Outline each blood parasite and name the species.
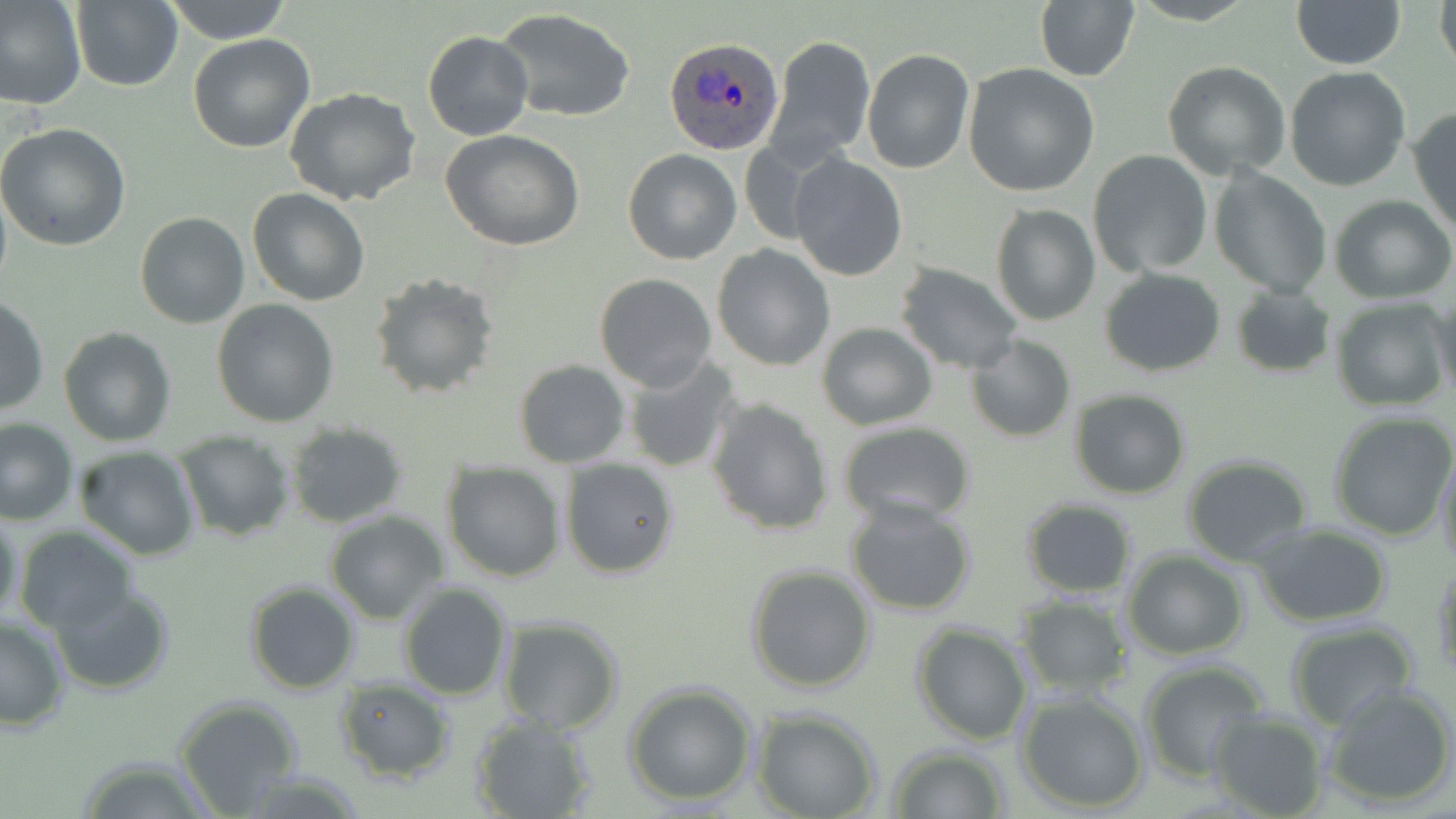

Approximate bounding boxes as named x1/y1/x2/y2 corners in pixels.
Plasmodium ovale-infected red blood cells: (x1=664, y1=37, x2=785, y2=156).
No Plasmodium falciparum, Plasmodium malariae, Plasmodium vivax, Babesia divergens, or Trypanosoma brucei observed.

Uninfected red blood cell locations: (x1=0, y1=0, x2=87, y2=109), (x1=162, y1=0, x2=295, y2=45), (x1=1035, y1=0, x2=1140, y2=83), (x1=1291, y1=0, x2=1405, y2=69), (x1=1433, y1=0, x2=1455, y2=81), (x1=70, y1=1, x2=183, y2=90), (x1=496, y1=8, x2=636, y2=123), (x1=423, y1=32, x2=533, y2=141), (x1=187, y1=34, x2=315, y2=153), (x1=767, y1=35, x2=875, y2=165), (x1=862, y1=49, x2=974, y2=174), (x1=1162, y1=61, x2=1291, y2=182), (x1=963, y1=65, x2=1100, y2=196), (x1=1284, y1=66, x2=1412, y2=192), (x1=284, y1=86, x2=422, y2=206), (x1=1409, y1=108, x2=1456, y2=236), (x1=0, y1=122, x2=131, y2=251), (x1=441, y1=128, x2=585, y2=250), (x1=623, y1=148, x2=741, y2=264), (x1=1087, y1=150, x2=1214, y2=279), (x1=789, y1=154, x2=907, y2=281), (x1=1209, y1=167, x2=1330, y2=299), (x1=247, y1=187, x2=370, y2=307), (x1=1331, y1=197, x2=1455, y2=303), (x1=989, y1=202, x2=1101, y2=327), (x1=135, y1=212, x2=249, y2=329), (x1=711, y1=244, x2=834, y2=371), (x1=895, y1=263, x2=1024, y2=376), (x1=1099, y1=267, x2=1226, y2=376), (x1=368, y1=271, x2=498, y2=398), (x1=594, y1=274, x2=717, y2=393), (x1=1230, y1=285, x2=1335, y2=379), (x1=1431, y1=291, x2=1456, y2=404), (x1=0, y1=295, x2=49, y2=417), (x1=212, y1=298, x2=341, y2=427), (x1=1332, y1=298, x2=1452, y2=410), (x1=816, y1=322, x2=937, y2=431), (x1=58, y1=327, x2=176, y2=445), (x1=966, y1=336, x2=1076, y2=442), (x1=622, y1=357, x2=743, y2=475), (x1=513, y1=359, x2=630, y2=468), (x1=1069, y1=387, x2=1191, y2=500), (x1=706, y1=398, x2=834, y2=536), (x1=1325, y1=411, x2=1456, y2=540), (x1=0, y1=418, x2=77, y2=525), (x1=284, y1=422, x2=410, y2=529), (x1=836, y1=423, x2=977, y2=527), (x1=175, y1=433, x2=295, y2=542), (x1=73, y1=446, x2=200, y2=562), (x1=1435, y1=446, x2=1456, y2=572), (x1=1181, y1=453, x2=1315, y2=566), (x1=559, y1=457, x2=680, y2=580), (x1=441, y1=461, x2=566, y2=583), (x1=845, y1=497, x2=976, y2=616), (x1=1020, y1=499, x2=1136, y2=598), (x1=0, y1=506, x2=23, y2=632), (x1=323, y1=512, x2=449, y2=623), (x1=1252, y1=524, x2=1394, y2=626), (x1=15, y1=527, x2=135, y2=635), (x1=1122, y1=551, x2=1248, y2=659), (x1=1432, y1=560, x2=1456, y2=681), (x1=745, y1=563, x2=878, y2=694), (x1=244, y1=580, x2=361, y2=695), (x1=397, y1=582, x2=513, y2=701), (x1=51, y1=585, x2=175, y2=696), (x1=1014, y1=594, x2=1131, y2=697), (x1=0, y1=614, x2=71, y2=733), (x1=497, y1=617, x2=625, y2=734), (x1=1284, y1=622, x2=1423, y2=731), (x1=912, y1=623, x2=1033, y2=745), (x1=1138, y1=660, x2=1271, y2=780), (x1=331, y1=678, x2=455, y2=784), (x1=623, y1=683, x2=758, y2=807), (x1=1323, y1=684, x2=1456, y2=807), (x1=1015, y1=690, x2=1149, y2=811), (x1=174, y1=696, x2=305, y2=815), (x1=753, y1=710, x2=879, y2=819), (x1=1207, y1=710, x2=1330, y2=818), (x1=469, y1=714, x2=597, y2=819), (x1=886, y1=745, x2=1009, y2=818), (x1=74, y1=754, x2=218, y2=819). Slide-level diagnosis: Plasmodium ovale. Image is 1456×819 pixels. Light microscopy. Captured at 1000x magnification. Thin blood film. May-Grünwald-Giemsa stain. Single field of view.